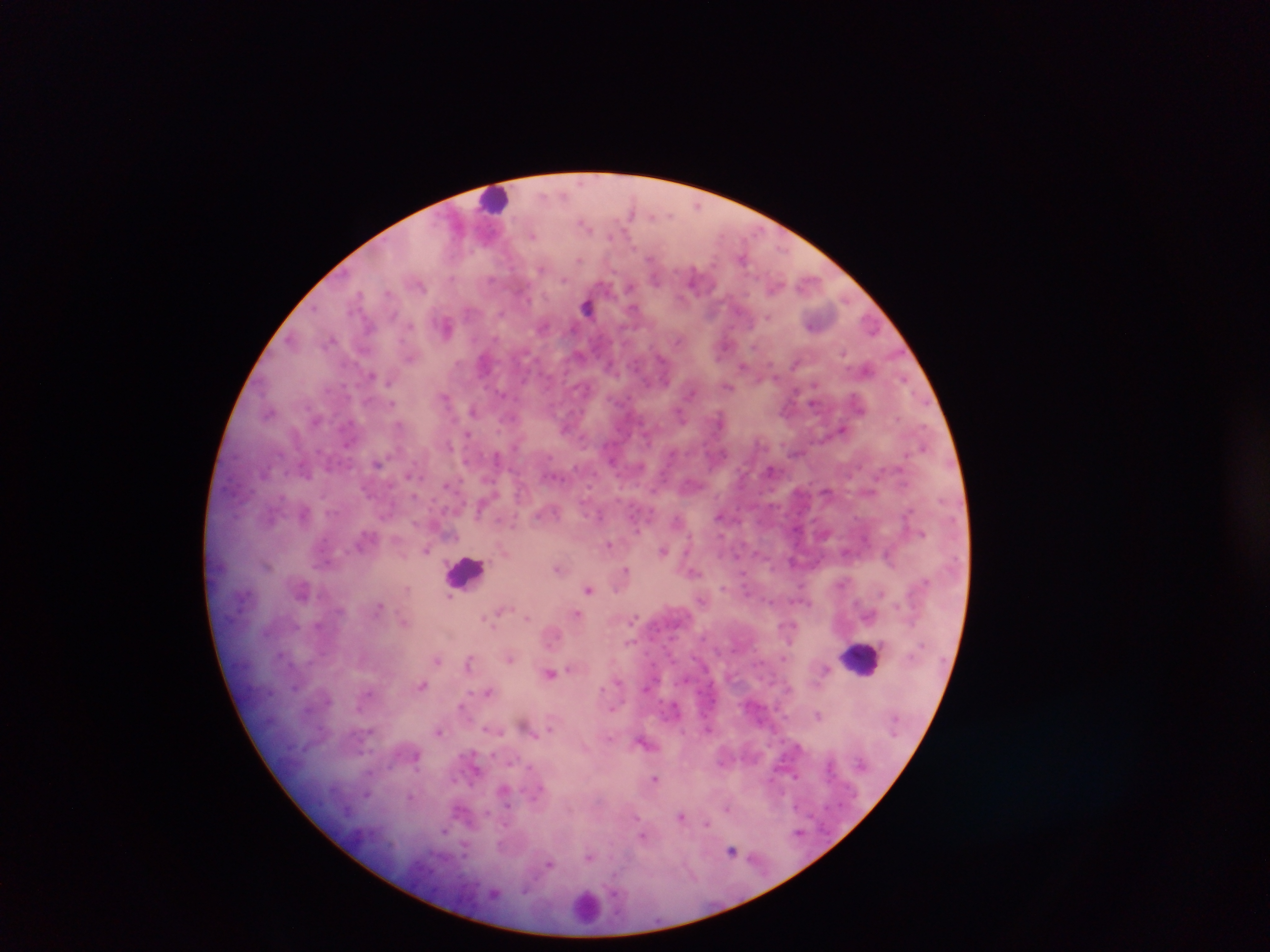
country = Ghana
image size = 1270×952 pixels
leukocyte locations = approximate centers as (x, y) in pixels: (497, 203), (467, 575), (857, 664), (586, 910)
malaria parasite locations = approximate centers as (x, y) in pixels: (583, 223), (533, 235), (579, 259), (542, 267), (564, 280), (422, 286), (587, 304), (409, 325), (447, 327), (679, 339), (744, 365), (902, 382), (729, 387), (504, 392), (690, 393), (445, 396), (393, 405), (474, 410), (679, 413), (719, 413), (512, 416), (400, 425), (842, 428), (469, 434), (447, 440), (673, 453), (496, 457), (612, 461), (378, 463), (772, 470), (307, 473), (408, 476), (448, 487), (416, 498), (584, 498), (332, 513), (304, 514), (677, 521), (514, 523), (636, 526), (922, 533), (609, 543), (663, 548), (427, 549), (846, 553), (889, 555), (792, 561), (267, 566), (626, 566), (559, 568), (743, 578), (845, 582), (725, 588), (407, 589), (588, 590), (882, 591), (451, 599), (771, 600), (380, 607), (577, 612), (872, 612), (496, 613), (488, 617), (527, 617), (635, 617), (405, 621), (294, 624), (318, 624), (793, 626), (553, 636), (706, 637), (629, 643), (470, 654), (281, 656), (438, 660), (471, 660), (510, 660), (572, 667), (550, 672), (621, 681), (296, 686), (423, 686), (645, 687), (602, 688), (489, 691), (464, 694), (462, 707), (616, 707), (359, 708), (818, 715), (487, 727), (550, 727), (440, 732), (533, 733), (610, 735), (644, 742), (476, 770), (798, 775), (655, 779), (455, 780), (540, 789), (367, 795), (409, 796), (456, 809), (728, 809), (637, 816), (680, 816), (707, 822), (444, 830), (799, 831), (643, 834), (465, 847), (732, 850), (589, 857), (549, 863), (495, 892), (616, 892)
field of view = single
capture = mobile-phone photograph through a microscope
preparation = thick blood smear